Name the blood parasite species.
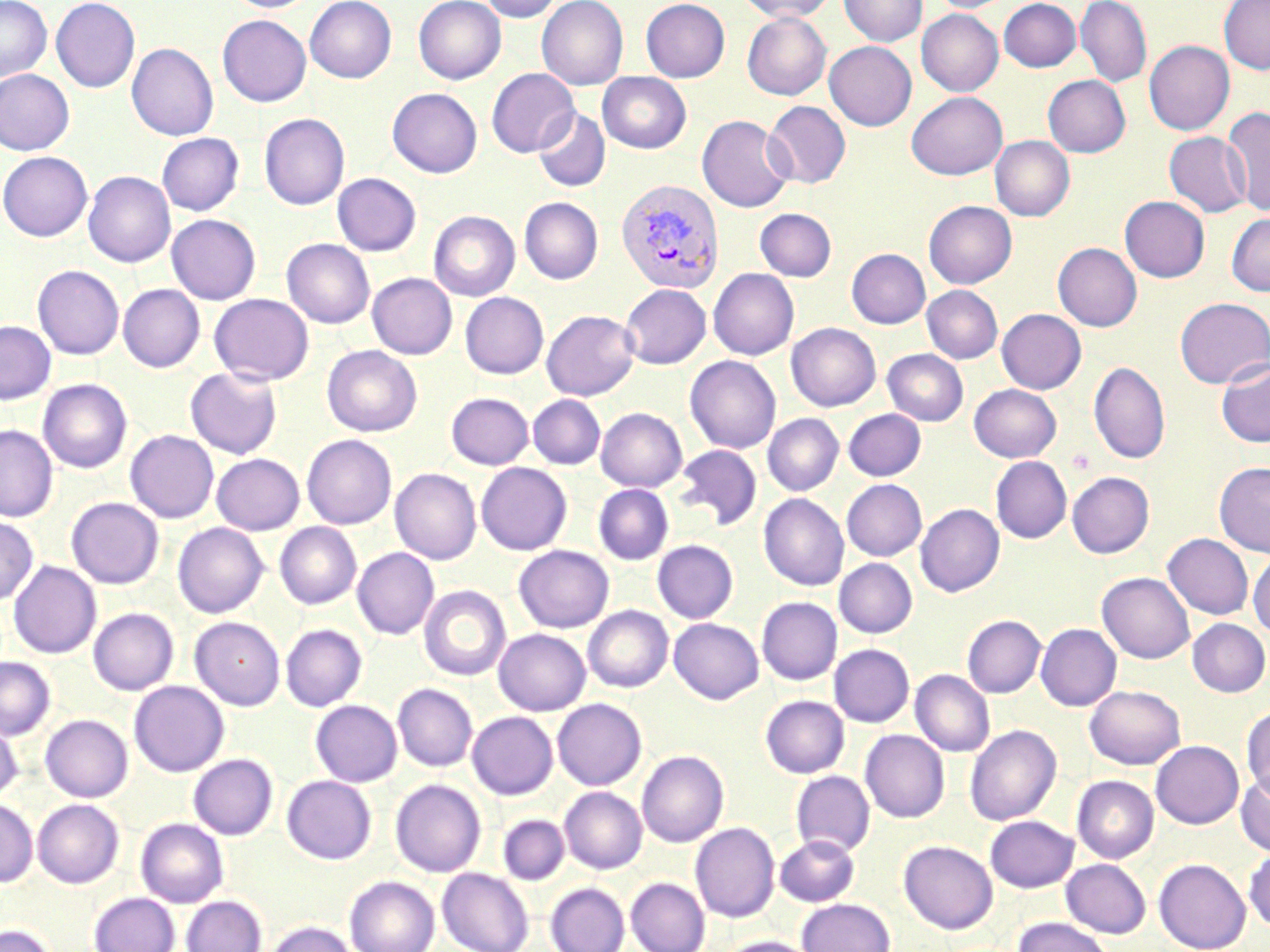
Plasmodium vivax.

Approximate bounding boxes as named x1/y1/x2/y2 corners in pixels. Uninfected red blood cell locations: (x1=0, y1=0, x2=52, y2=81), (x1=51, y1=0, x2=140, y2=92), (x1=225, y1=0, x2=317, y2=12), (x1=305, y1=0, x2=396, y2=83), (x1=413, y1=0, x2=506, y2=84), (x1=478, y1=0, x2=564, y2=22), (x1=536, y1=0, x2=629, y2=90), (x1=640, y1=0, x2=730, y2=82), (x1=737, y1=0, x2=837, y2=22), (x1=840, y1=0, x2=927, y2=46), (x1=929, y1=0, x2=1015, y2=13), (x1=998, y1=0, x2=1082, y2=72), (x1=1076, y1=0, x2=1152, y2=88), (x1=1219, y1=0, x2=1270, y2=74), (x1=916, y1=9, x2=1003, y2=96), (x1=742, y1=12, x2=831, y2=100), (x1=217, y1=15, x2=311, y2=106), (x1=1144, y1=40, x2=1234, y2=135), (x1=824, y1=41, x2=916, y2=130), (x1=127, y1=43, x2=218, y2=140), (x1=486, y1=68, x2=579, y2=157), (x1=0, y1=70, x2=74, y2=155), (x1=597, y1=72, x2=692, y2=153), (x1=1043, y1=75, x2=1130, y2=157), (x1=387, y1=88, x2=482, y2=177), (x1=906, y1=92, x2=1007, y2=180), (x1=763, y1=101, x2=850, y2=189), (x1=1222, y1=107, x2=1270, y2=215), (x1=533, y1=109, x2=610, y2=192), (x1=259, y1=113, x2=350, y2=210), (x1=696, y1=115, x2=794, y2=212), (x1=1164, y1=132, x2=1251, y2=217), (x1=157, y1=133, x2=244, y2=215), (x1=990, y1=136, x2=1075, y2=221), (x1=0, y1=151, x2=92, y2=241), (x1=0, y1=161, x2=175, y2=250), (x1=83, y1=171, x2=176, y2=267), (x1=332, y1=173, x2=421, y2=256), (x1=1120, y1=196, x2=1210, y2=282), (x1=519, y1=197, x2=603, y2=284), (x1=924, y1=200, x2=1017, y2=288), (x1=755, y1=208, x2=837, y2=281), (x1=428, y1=211, x2=520, y2=302), (x1=1226, y1=212, x2=1270, y2=297), (x1=166, y1=214, x2=261, y2=304), (x1=281, y1=238, x2=375, y2=328), (x1=1053, y1=242, x2=1142, y2=331), (x1=846, y1=249, x2=930, y2=328), (x1=33, y1=265, x2=124, y2=359), (x1=708, y1=268, x2=799, y2=359), (x1=367, y1=273, x2=457, y2=359), (x1=118, y1=284, x2=205, y2=372), (x1=619, y1=284, x2=711, y2=368), (x1=921, y1=285, x2=1003, y2=363), (x1=460, y1=292, x2=548, y2=379), (x1=209, y1=293, x2=314, y2=385), (x1=1175, y1=297, x2=1270, y2=388), (x1=997, y1=309, x2=1086, y2=394), (x1=541, y1=310, x2=640, y2=400), (x1=0, y1=321, x2=56, y2=404), (x1=786, y1=323, x2=881, y2=411), (x1=322, y1=345, x2=422, y2=436), (x1=882, y1=349, x2=968, y2=425), (x1=685, y1=355, x2=781, y2=454), (x1=1216, y1=358, x2=1270, y2=448), (x1=1089, y1=362, x2=1171, y2=464), (x1=185, y1=366, x2=283, y2=460), (x1=38, y1=379, x2=132, y2=473), (x1=969, y1=384, x2=1061, y2=462), (x1=446, y1=392, x2=534, y2=469), (x1=528, y1=395, x2=605, y2=469), (x1=596, y1=408, x2=687, y2=492), (x1=843, y1=409, x2=926, y2=480), (x1=762, y1=413, x2=843, y2=496), (x1=0, y1=425, x2=58, y2=521), (x1=125, y1=430, x2=219, y2=523), (x1=301, y1=435, x2=396, y2=529), (x1=674, y1=445, x2=762, y2=530), (x1=211, y1=453, x2=305, y2=535), (x1=991, y1=456, x2=1072, y2=543), (x1=476, y1=462, x2=572, y2=555), (x1=1214, y1=462, x2=1270, y2=557), (x1=390, y1=468, x2=481, y2=564), (x1=1067, y1=471, x2=1154, y2=558), (x1=841, y1=479, x2=927, y2=561), (x1=593, y1=484, x2=674, y2=565), (x1=759, y1=493, x2=849, y2=590), (x1=66, y1=497, x2=164, y2=589), (x1=915, y1=504, x2=1004, y2=597), (x1=0, y1=515, x2=38, y2=605), (x1=173, y1=522, x2=268, y2=617), (x1=274, y1=522, x2=361, y2=609), (x1=1163, y1=533, x2=1253, y2=619), (x1=652, y1=540, x2=738, y2=623), (x1=514, y1=545, x2=614, y2=633), (x1=352, y1=548, x2=439, y2=639), (x1=1248, y1=553, x2=1270, y2=637), (x1=834, y1=558, x2=917, y2=637), (x1=8, y1=560, x2=101, y2=659), (x1=1097, y1=572, x2=1194, y2=663), (x1=418, y1=585, x2=511, y2=681), (x1=756, y1=597, x2=842, y2=685), (x1=583, y1=605, x2=673, y2=692), (x1=88, y1=608, x2=179, y2=695), (x1=962, y1=615, x2=1046, y2=697), (x1=190, y1=617, x2=285, y2=710), (x1=669, y1=618, x2=763, y2=704), (x1=1187, y1=618, x2=1270, y2=697), (x1=280, y1=624, x2=367, y2=711), (x1=1036, y1=624, x2=1121, y2=711), (x1=493, y1=628, x2=591, y2=715), (x1=829, y1=644, x2=914, y2=727), (x1=0, y1=657, x2=55, y2=740), (x1=910, y1=670, x2=995, y2=756), (x1=129, y1=680, x2=229, y2=777), (x1=392, y1=683, x2=478, y2=771), (x1=1085, y1=685, x2=1185, y2=769), (x1=760, y1=695, x2=849, y2=778), (x1=552, y1=698, x2=647, y2=790), (x1=311, y1=700, x2=402, y2=787), (x1=1241, y1=705, x2=1270, y2=800), (x1=467, y1=711, x2=558, y2=799), (x1=40, y1=714, x2=133, y2=802), (x1=0, y1=717, x2=23, y2=803), (x1=965, y1=724, x2=1062, y2=825), (x1=860, y1=729, x2=949, y2=822), (x1=1151, y1=740, x2=1243, y2=828), (x1=637, y1=750, x2=728, y2=847), (x1=188, y1=754, x2=278, y2=839), (x1=791, y1=771, x2=875, y2=856), (x1=1236, y1=772, x2=1270, y2=856), (x1=282, y1=775, x2=376, y2=864), (x1=1072, y1=775, x2=1159, y2=863), (x1=390, y1=779, x2=486, y2=877), (x1=559, y1=786, x2=647, y2=873), (x1=0, y1=799, x2=38, y2=887), (x1=32, y1=799, x2=124, y2=888), (x1=498, y1=815, x2=569, y2=884), (x1=985, y1=815, x2=1078, y2=892), (x1=136, y1=818, x2=228, y2=907), (x1=690, y1=822, x2=780, y2=922), (x1=775, y1=835, x2=859, y2=906), (x1=899, y1=840, x2=998, y2=934), (x1=1244, y1=848, x2=1270, y2=931), (x1=1154, y1=858, x2=1251, y2=952), (x1=1061, y1=859, x2=1151, y2=938), (x1=437, y1=868, x2=534, y2=952), (x1=344, y1=876, x2=440, y2=952), (x1=626, y1=878, x2=710, y2=952), (x1=545, y1=882, x2=630, y2=952), (x1=89, y1=892, x2=180, y2=952), (x1=181, y1=895, x2=266, y2=952), (x1=797, y1=899, x2=895, y2=952), (x1=1013, y1=917, x2=1115, y2=952), (x1=263, y1=921, x2=357, y2=952), (x1=0, y1=923, x2=56, y2=952), (x1=718, y1=935, x2=818, y2=952). Plasmodium vivax-infected red blood cell locations: (x1=616, y1=179, x2=724, y2=294). May-Grünwald-Giemsa-stained preparation. Image is 1270×952 pixels. Captured at 1000x magnification. Thin blood smear. One field of a larger specimen. Light microscopy.